Describe the morphology of the red blood cells.
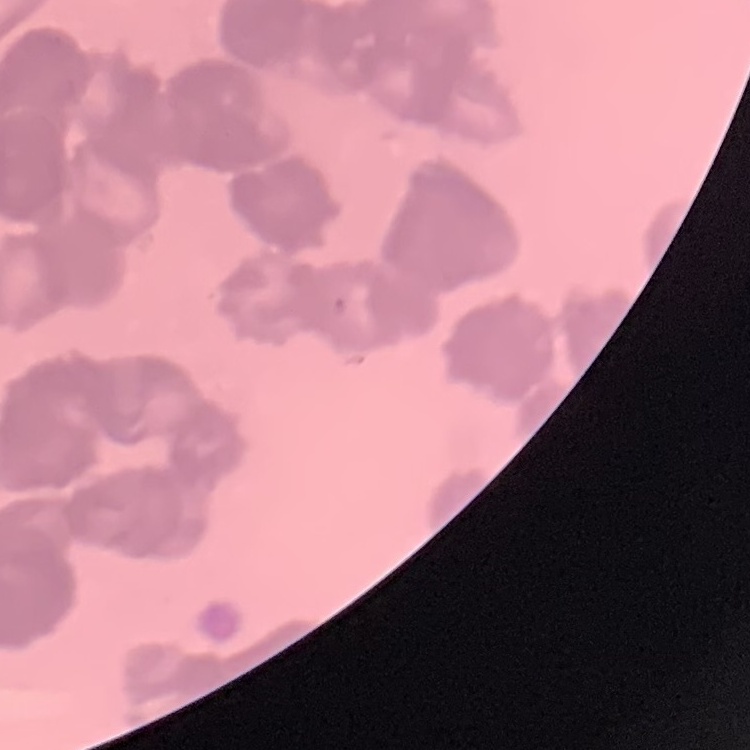

They show rouleaux formation.

Square crop of a larger photomicrograph. Field's or Giemsa stain. Thin blood film.